Classify this cell by malaria status.
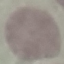
Uninfected.

Summary:
  - Image type: cell patch, automatically extracted from a larger field of view and resized to 64 × 64 pixels
  - Preparation: thin smear
  - Stain: Giemsa
  - Capture: smartphone through the microscope eyepiece